Describe the morphology of the erythrocytes.
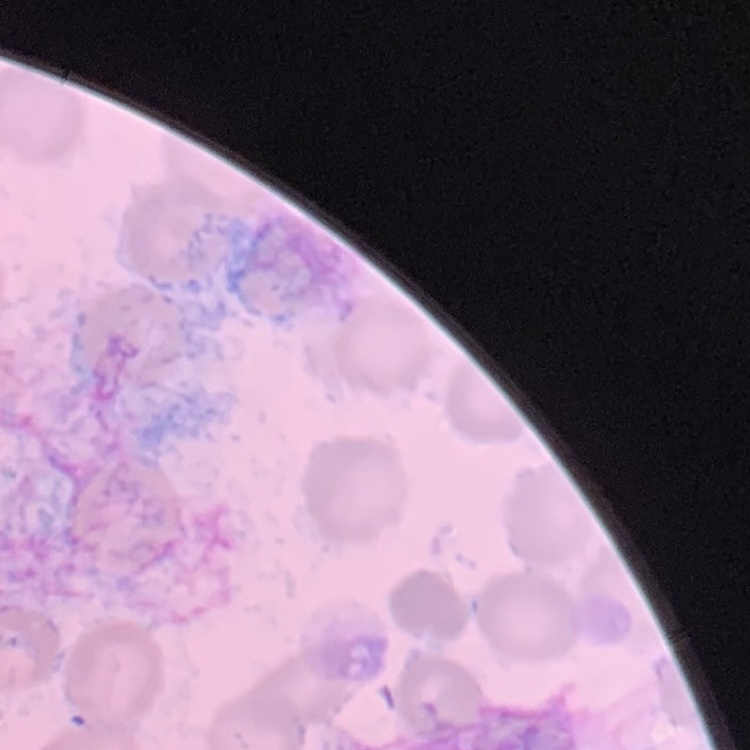
They show no rouleaux formation.

preparation = thin peripheral smear
stain = Field's or Giemsa
image type = one tile cut from a larger photomicrograph